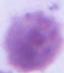

magnification: 1000x
modality: micrograph
identification: red blood cell